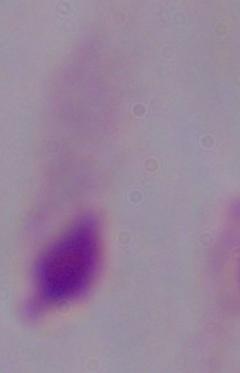
Summary:
  - Identification: trichomonad
  - Magnification: 1000x
  - Modality: photomicrograph